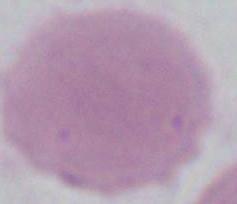
magnification = 1000x
identification = erythrocyte
modality = photomicrograph